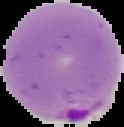
image size = 124×127 pixels
result = malaria parasites identified
preparation = thin blood smear
image type = segmented cell region on a black background